State which cell type is depicted.
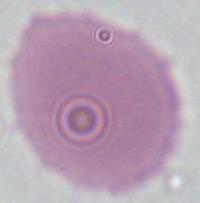

This is an erythrocyte.

modality = micrograph
magnification = 1000x